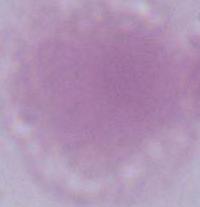 Micrograph. A red blood cell is shown. 1000x magnification.